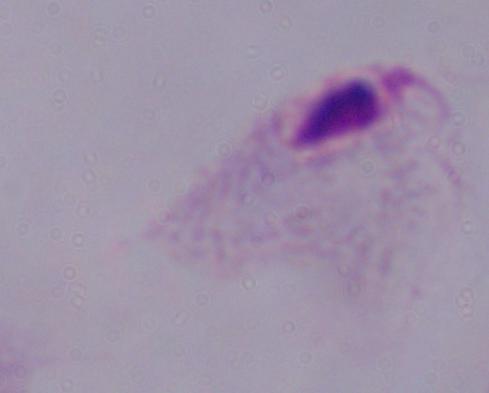

Micrograph. A trichomonad is shown. 1000x magnification.